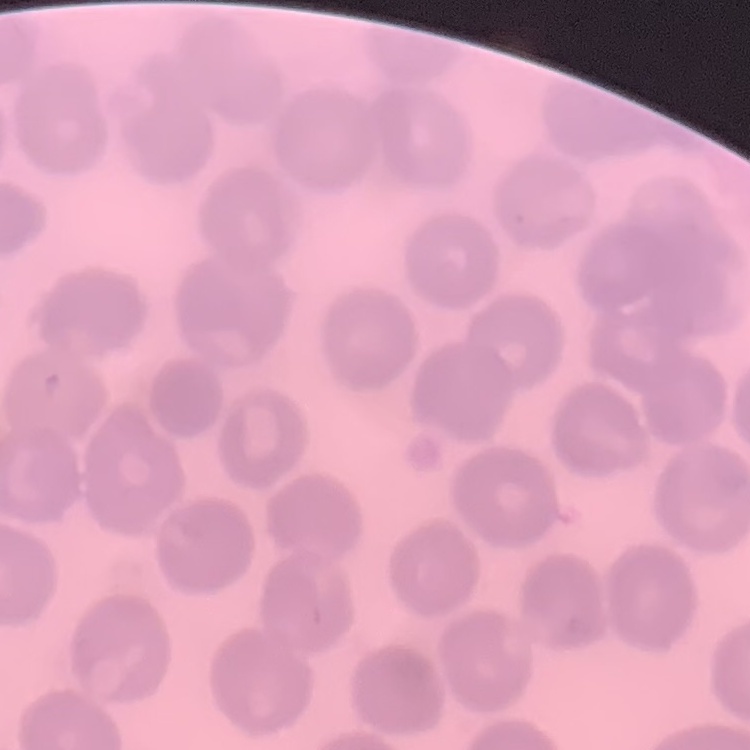

Summary:
  - Erythrocyte morphology: no rouleaux formation
  - Image type: one tile cut from a larger photomicrograph
  - Stain: Field's or Giemsa
  - Preparation: thin peripheral smear